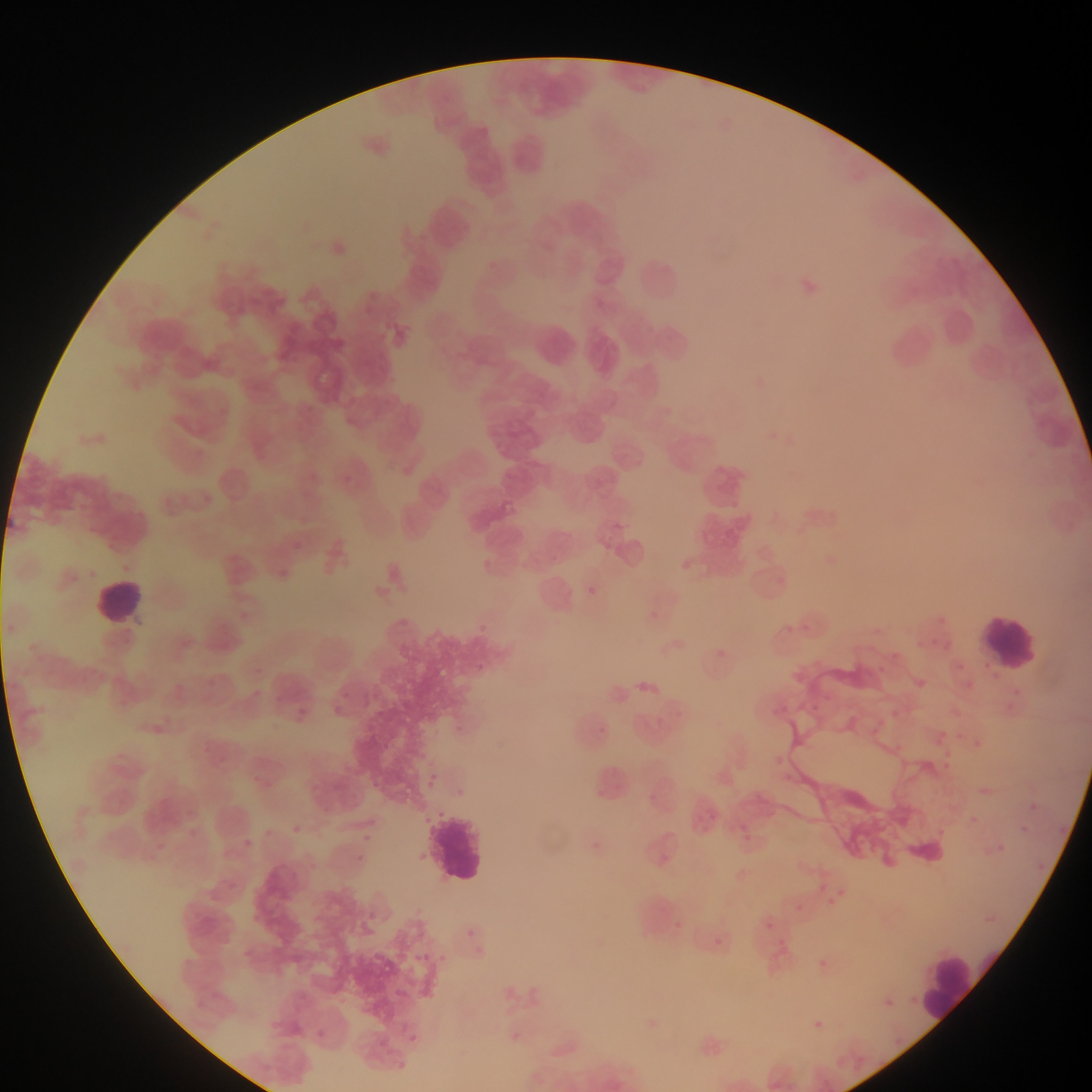

country = Ghana
field of view = single
leukocyte locations = approximate bounding boxes as {left, top, right, bottom} in pixels: {91, 577, 148, 634}, {981, 609, 1044, 668}, {430, 806, 490, 890}, {922, 951, 983, 1025}
image size = 1092×1092 pixels
Plasmodium parasite locations = approximate bounding boxes as {left, top, right, bottom} in pixels: {341, 475, 350, 483}, {293, 539, 302, 548}, {280, 569, 289, 578}, {582, 583, 599, 598}, {483, 618, 499, 639}, {472, 661, 486, 673}, {636, 675, 657, 700}, {331, 686, 352, 698}, {329, 706, 342, 715}, {601, 719, 611, 738}, {423, 770, 437, 787}, {591, 787, 612, 804}, {642, 790, 659, 804}, {706, 808, 724, 833}, {357, 810, 384, 830}, {291, 821, 310, 838}, {738, 821, 750, 835}, {254, 825, 273, 840}, {366, 827, 377, 849}, {415, 847, 431, 867}, {351, 851, 365, 863}, {814, 871, 826, 890}, {797, 895, 808, 915}, {830, 897, 844, 914}, {365, 907, 377, 916}, {763, 917, 782, 942}, {462, 923, 474, 939}, {715, 934, 731, 950}, {777, 940, 789, 953}, {420, 944, 440, 964}, {819, 954, 835, 964}, {403, 974, 429, 990}, {911, 989, 921, 1011}, {885, 991, 902, 1014}, {335, 993, 349, 1008}, {817, 1017, 829, 1032}, {309, 1021, 332, 1041}, {405, 1032, 417, 1046}, {378, 1034, 392, 1048}, {394, 1053, 410, 1075}
preparation = thin blood film
capture = mobile-phone photograph through a microscope